Assess this cell for malaria.
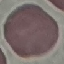

Uninfected.

Automatically extracted cell patch, resized to 64 × 64 pixels. Photographed with a smartphone camera at the microscope eyepiece. Giemsa stain. Thin blood smear.